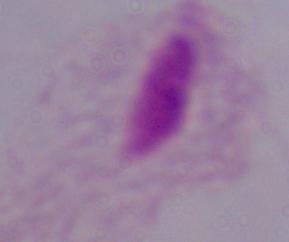
Summary:
  - Magnification: 1000x
  - Identification: trichomonad
  - Modality: photomicrograph